Evaluate for malaria.
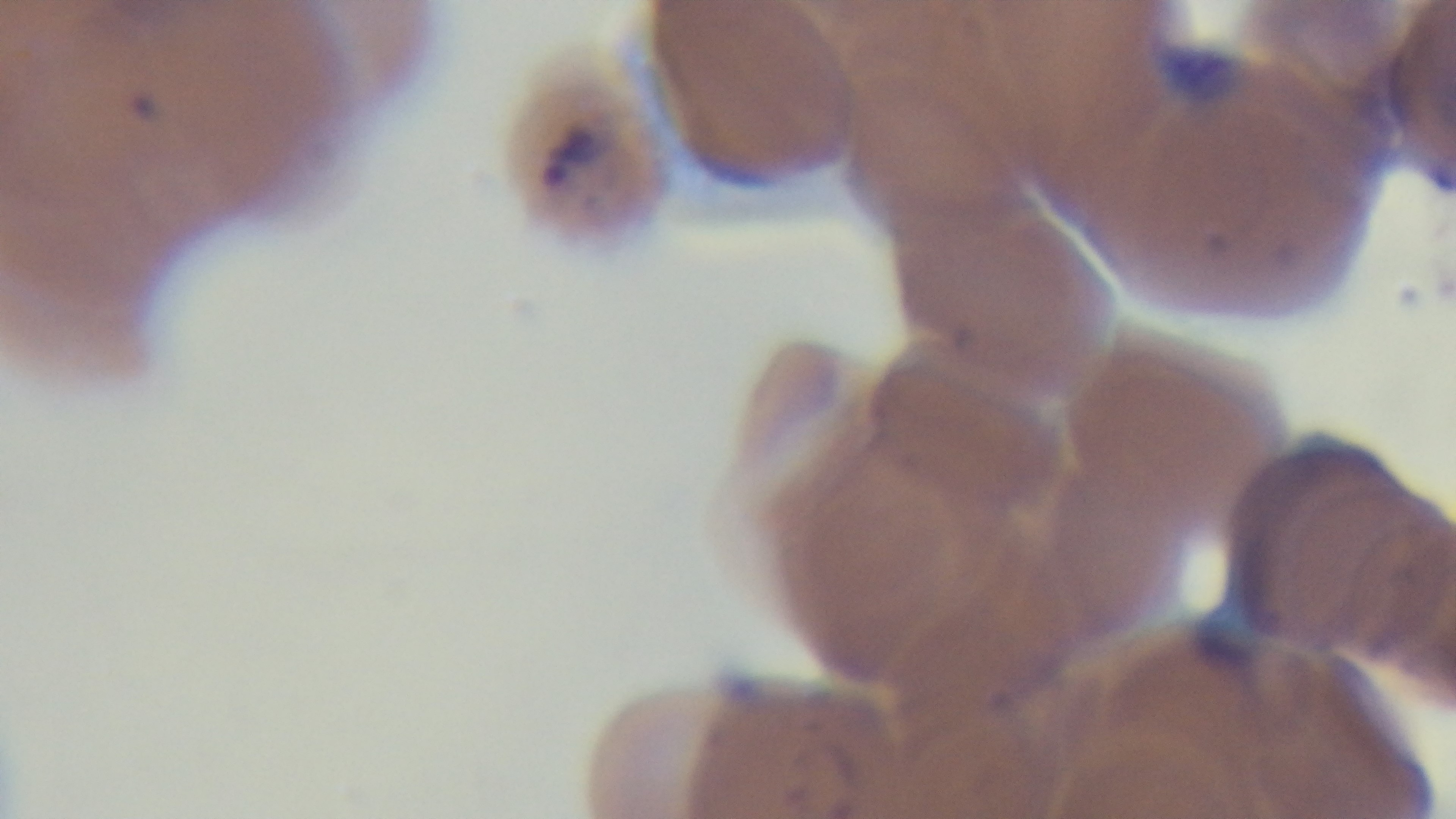
It is infected.

objective: 100x oil immersion
capture: mounted 4K digital camera
stain: Giemsa
preparation: thin blood film
field_of_view: one from the slide
modality: light microscopy